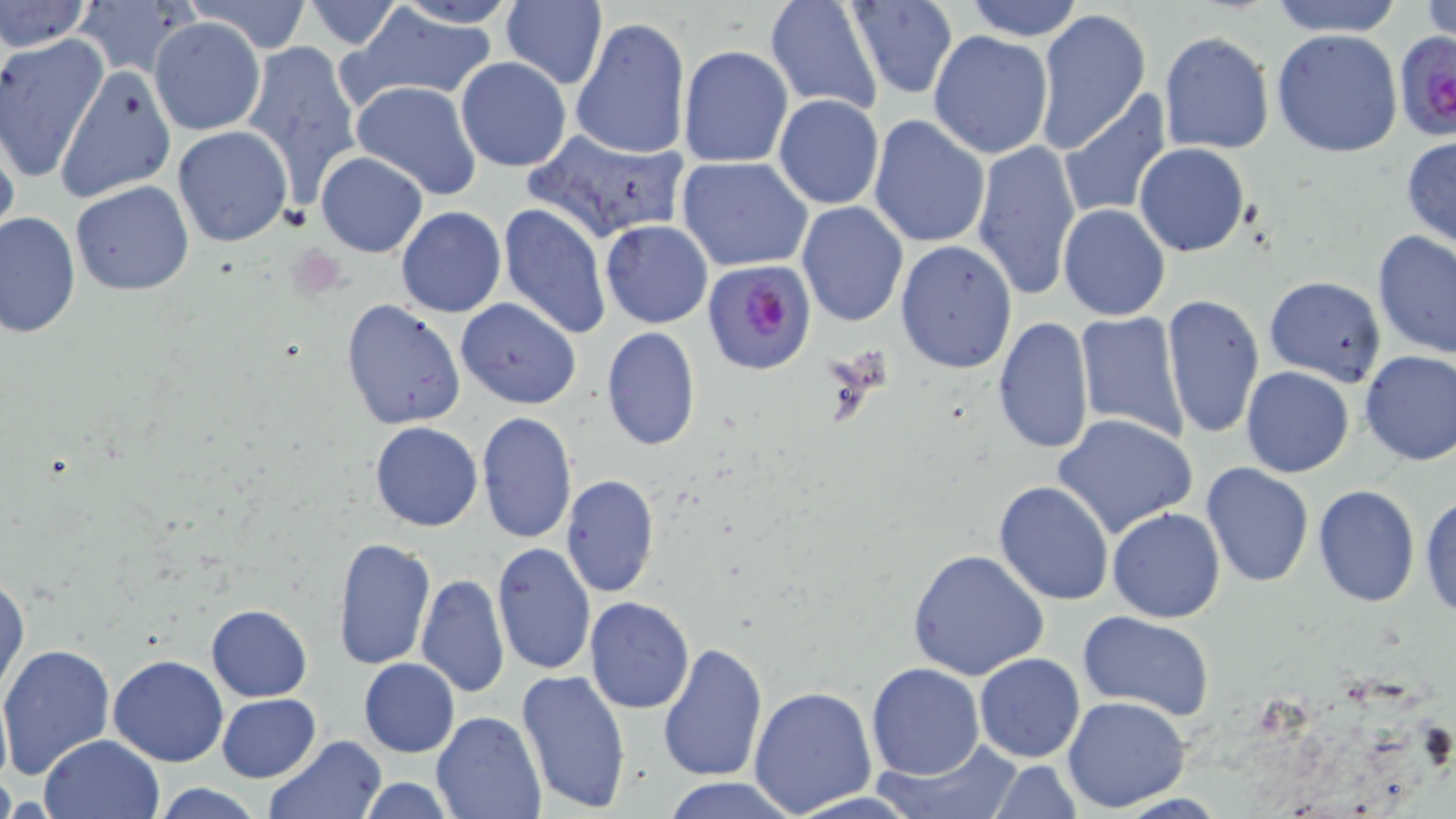
Summary:
  - Coordinate format: approximate bounding boxes as (x1, y1, x2, y2) in pixels
  - Uninfected red blood cell locations: (72, 0, 198, 78), (185, 0, 313, 52), (299, 0, 404, 50), (387, 0, 517, 28), (501, 0, 608, 90), (963, 0, 1085, 41), (1268, 0, 1403, 37), (1422, 0, 1455, 43), (0, 1, 90, 54), (761, 2, 882, 116), (844, 2, 958, 101), (348, 6, 499, 101), (1034, 7, 1152, 153), (572, 16, 691, 160), (148, 17, 267, 137), (1272, 29, 1404, 158), (928, 31, 1054, 159), (1158, 31, 1274, 155), (0, 35, 109, 184), (240, 40, 363, 198), (677, 44, 793, 168), (455, 57, 572, 172), (53, 63, 178, 204), (350, 80, 482, 201), (1057, 92, 1174, 221), (773, 95, 884, 210), (868, 114, 991, 249), (0, 121, 20, 249), (172, 126, 293, 247), (524, 126, 692, 242), (1401, 136, 1456, 249), (971, 139, 1082, 299), (1134, 143, 1249, 256), (314, 151, 428, 258), (677, 157, 814, 273), (70, 181, 195, 296), (797, 201, 908, 327), (498, 202, 611, 338), (1057, 204, 1171, 321), (395, 207, 506, 317), (0, 212, 80, 340), (600, 221, 712, 329), (1372, 230, 1456, 360), (895, 239, 1017, 373), (1263, 276, 1385, 385), (1162, 292, 1265, 437), (340, 298, 467, 432), (455, 298, 581, 408), (1075, 311, 1191, 446), (994, 317, 1094, 453), (601, 326, 702, 451), (1358, 350, 1456, 467), (1241, 366, 1355, 478), (476, 412, 577, 544), (1052, 413, 1200, 542), (369, 420, 482, 532), (1200, 462, 1316, 587), (559, 474, 660, 599), (993, 480, 1112, 606), (1313, 484, 1422, 607), (1420, 490, 1455, 623), (1107, 508, 1225, 624), (331, 538, 436, 671), (492, 542, 597, 676), (907, 549, 1049, 683), (1, 573, 27, 700), (416, 573, 509, 697), (585, 597, 696, 713), (207, 603, 313, 701), (1077, 611, 1214, 719), (659, 642, 768, 782), (0, 644, 119, 782), (973, 653, 1085, 763), (108, 654, 230, 766), (359, 658, 459, 757), (865, 663, 986, 781), (516, 669, 633, 814), (749, 685, 878, 815), (0, 687, 11, 793), (216, 694, 320, 782), (1061, 695, 1190, 814), (432, 711, 544, 819), (40, 735, 165, 819), (263, 737, 386, 819), (880, 738, 1025, 817), (985, 762, 1085, 816), (662, 777, 803, 819), (354, 778, 458, 818), (148, 783, 270, 819)
  - Plasmodium falciparum-infected red blood cell locations: (1393, 34, 1456, 143), (701, 261, 816, 377)
  - Slide-level diagnosis: Plasmodium falciparum
  - Magnification: 1000x
  - Image size: 1456×819 pixels
  - Modality: optical microscopy
  - Field of view: single
  - Preparation: thin blood film
  - Stain: May-Grünwald-Giemsa